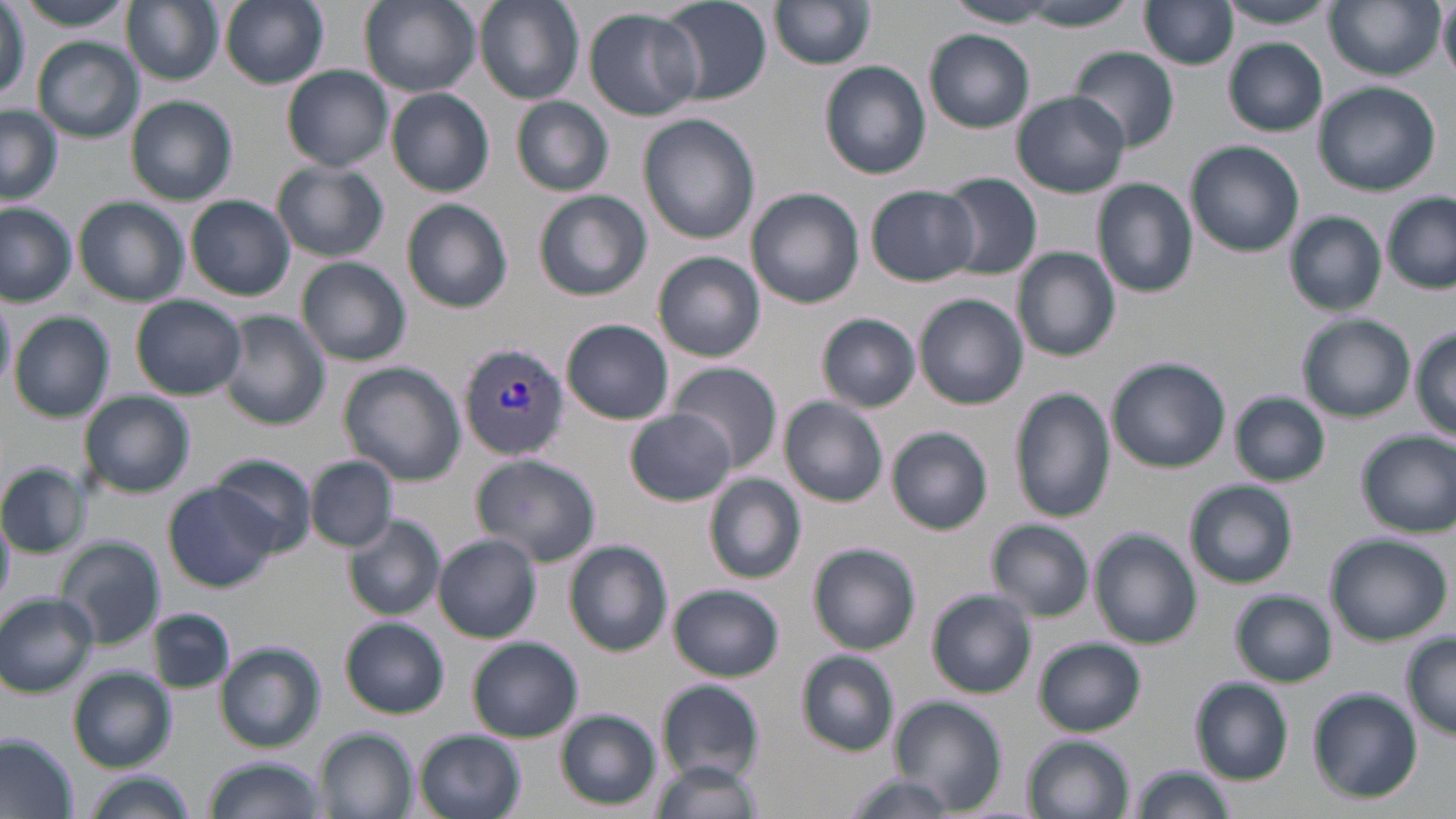
Summary:
  - Coordinate format: approximate bounding boxes as (x1,y1)-(x2,y2) corner pairs in pixels
  - Uninfected red blood cell locations: (17,0)-(138,31), (122,0)-(224,85), (221,0)-(329,89), (359,0)-(481,96), (475,0)-(584,105), (658,0)-(772,106), (1215,0)-(1341,29), (770,1)-(876,71), (1140,1)-(1240,69), (1439,1)-(1456,79), (943,2)-(1059,29), (1326,2)-(1442,80), (1017,3)-(1136,32), (0,5)-(27,104), (584,8)-(703,120), (925,29)-(1035,133), (34,37)-(143,142), (1224,40)-(1328,135), (1069,47)-(1180,152), (820,61)-(932,179), (283,65)-(393,171), (1313,82)-(1441,197), (387,89)-(495,196), (1010,90)-(1130,198), (125,95)-(238,205), (513,96)-(614,195), (0,105)-(61,206), (638,114)-(760,245), (1185,142)-(1304,256), (272,161)-(388,262), (939,172)-(1042,279), (1093,178)-(1197,298), (865,184)-(980,286), (747,189)-(864,309), (533,190)-(652,301), (1383,192)-(1456,292), (187,195)-(295,301), (74,197)-(189,306), (403,199)-(514,313), (0,201)-(77,306), (1284,212)-(1387,316), (1013,247)-(1120,362), (653,252)-(766,362), (298,257)-(411,365), (0,291)-(15,399), (915,294)-(1028,410), (130,295)-(246,400), (219,310)-(330,431), (9,312)-(114,422), (817,313)-(920,413), (1297,314)-(1414,422), (562,320)-(674,423), (1411,328)-(1456,437), (1108,358)-(1230,473), (667,362)-(781,473), (338,363)-(465,484), (1010,387)-(1117,524), (79,391)-(195,498), (1229,391)-(1331,486), (780,397)-(888,506), (627,409)-(736,506), (887,427)-(993,535), (1356,429)-(1456,537), (209,452)-(318,555), (472,453)-(601,567), (308,456)-(396,550), (0,462)-(91,558), (705,475)-(806,583), (1184,479)-(1298,588), (164,483)-(278,592), (0,511)-(15,604), (345,514)-(444,619), (988,520)-(1093,620), (1091,528)-(1201,650), (433,534)-(542,642), (1325,534)-(1453,642), (55,536)-(166,650), (565,541)-(673,657), (809,542)-(921,654), (670,585)-(785,681), (928,589)-(1038,698), (1231,590)-(1336,686), (0,592)-(100,697), (148,607)-(235,695), (341,618)-(450,718), (1401,635)-(1456,739), (468,636)-(582,742), (1035,637)-(1145,736), (217,644)-(325,753), (796,651)-(899,755), (69,668)-(175,770), (1190,678)-(1293,783), (656,679)-(766,781), (1306,688)-(1423,803), (886,697)-(1007,812), (554,709)-(661,810), (315,728)-(418,819), (415,730)-(526,819), (1025,734)-(1135,818), (0,735)-(75,819), (204,755)-(327,819), (648,758)-(760,819), (1129,764)-(1235,819), (81,772)-(196,819), (838,774)-(965,818)
  - Plasmodium vivax-infected red blood cell locations: (458,341)-(568,461)
  - Slide-level diagnosis: Plasmodium vivax
  - Image size: 1456×819 pixels
  - Field of view: one of a larger specimen
  - Modality: optical microscopy
  - Preparation: thin blood film
  - Magnification: 1000x
  - Stain: May-Grünwald-Giemsa